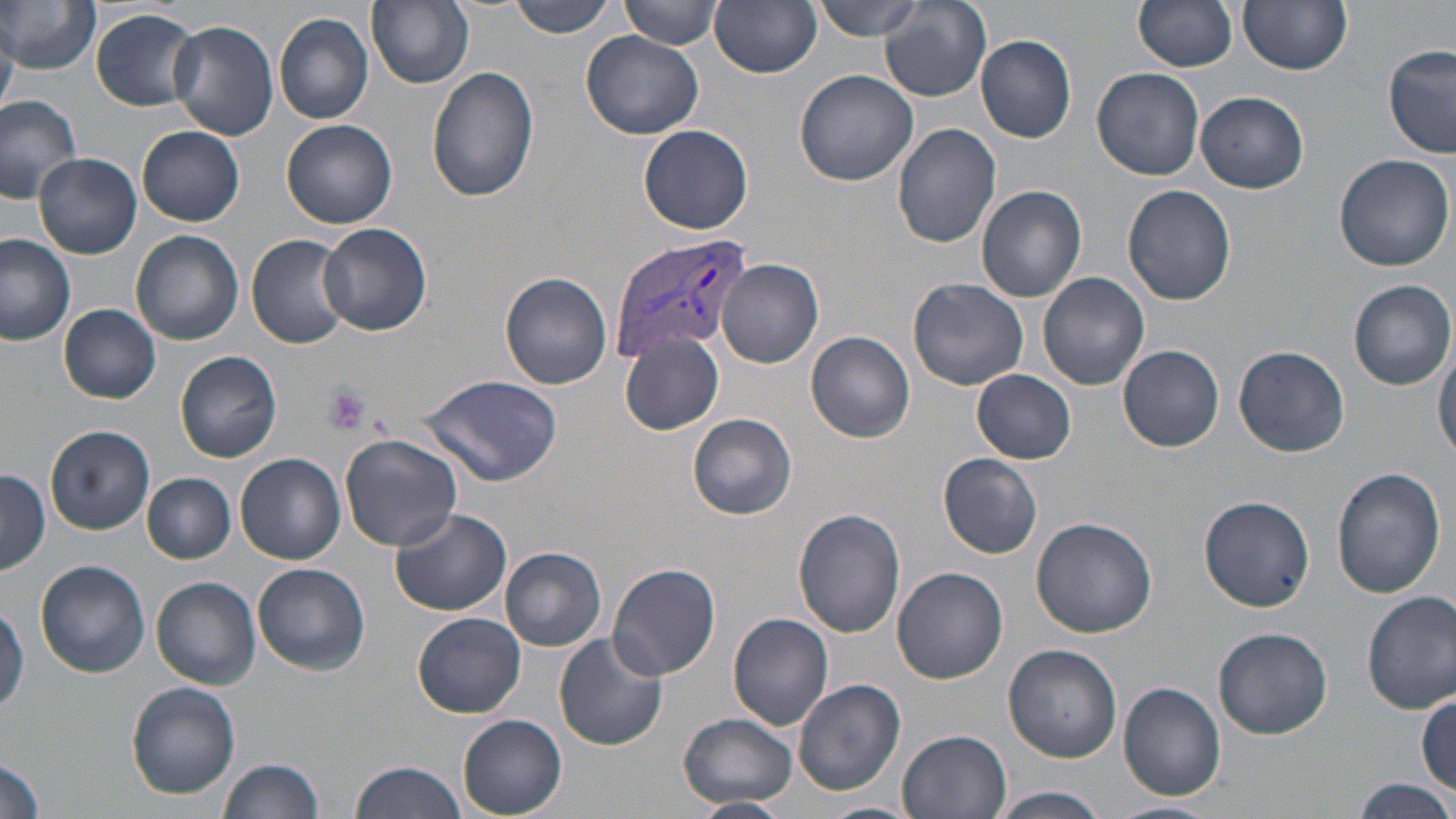

Approximate bounding boxes as (x1,y1)-(x2,y2) corner pairs in pixels. Uninfected red blood cell locations: (1,0)-(100,73), (504,0)-(620,38), (621,0)-(722,50), (810,0)-(930,41), (1137,0)-(1238,73), (1241,0)-(1353,74), (711,1)-(822,77), (368,2)-(474,89), (880,2)-(993,102), (90,9)-(202,111), (274,13)-(372,123), (168,21)-(279,140), (582,31)-(703,139), (976,35)-(1078,143), (1384,45)-(1456,159), (425,65)-(539,201), (1093,67)-(1204,180), (794,68)-(920,185), (1196,91)-(1309,193), (0,92)-(82,202), (282,119)-(397,228), (892,123)-(1002,248), (639,124)-(753,234), (137,125)-(245,226), (33,152)-(142,257), (1333,154)-(1455,272), (976,185)-(1087,302), (1121,185)-(1236,305), (318,222)-(432,336), (131,231)-(243,345), (0,234)-(76,345), (247,234)-(353,348), (717,259)-(823,367), (501,272)-(612,388), (1037,272)-(1150,391), (907,276)-(1029,390), (1350,281)-(1455,390), (58,304)-(162,402), (807,332)-(914,440), (619,333)-(724,436), (1433,335)-(1456,459), (1118,345)-(1224,452), (1234,345)-(1350,457), (175,350)-(282,462), (970,370)-(1076,464), (421,374)-(564,488), (688,413)-(797,519), (45,425)-(155,535), (339,434)-(463,551), (234,453)-(346,564), (939,454)-(1043,559), (1331,465)-(1447,598), (0,469)-(51,577), (143,473)-(236,563), (1200,496)-(1317,612), (388,506)-(511,616), (793,509)-(906,637), (1031,518)-(1157,638), (501,548)-(605,649), (35,559)-(153,678), (253,562)-(373,675), (608,563)-(720,679), (891,567)-(1008,683), (152,576)-(261,688), (1362,590)-(1456,714), (0,598)-(27,717), (413,612)-(527,718), (727,612)-(833,730), (1213,626)-(1333,739), (554,632)-(668,752), (1004,644)-(1122,764), (793,680)-(905,794), (126,681)-(240,798), (1117,681)-(1226,800), (1415,694)-(1455,794), (679,712)-(797,809), (458,714)-(566,817), (896,729)-(1011,819), (0,753)-(46,819), (219,758)-(326,818), (349,760)-(470,818), (1348,777)-(1456,817), (991,788)-(1111,819), (690,796)-(790,818), (1104,799)-(1216,819), (815,801)-(924,819). Platelet locations: (321,382)-(374,436). Plasmodium vivax-infected red blood cell locations: (608,230)-(754,358). Slide-level diagnosis: Plasmodium vivax. Image is 1456×819 pixels. Thin blood film. Single field of view. Optical microscopy. 1000x magnification. May-Grünwald-Giemsa-stained preparation.